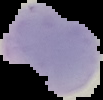

Summary:
  - Preparation: thin blood smear
  - Image size: 103×100 pixels
  - Result: Plasmodium parasites identified
  - Image type: cell region segmented out of the field of view; surrounding area masked to black